State the blood parasite species.
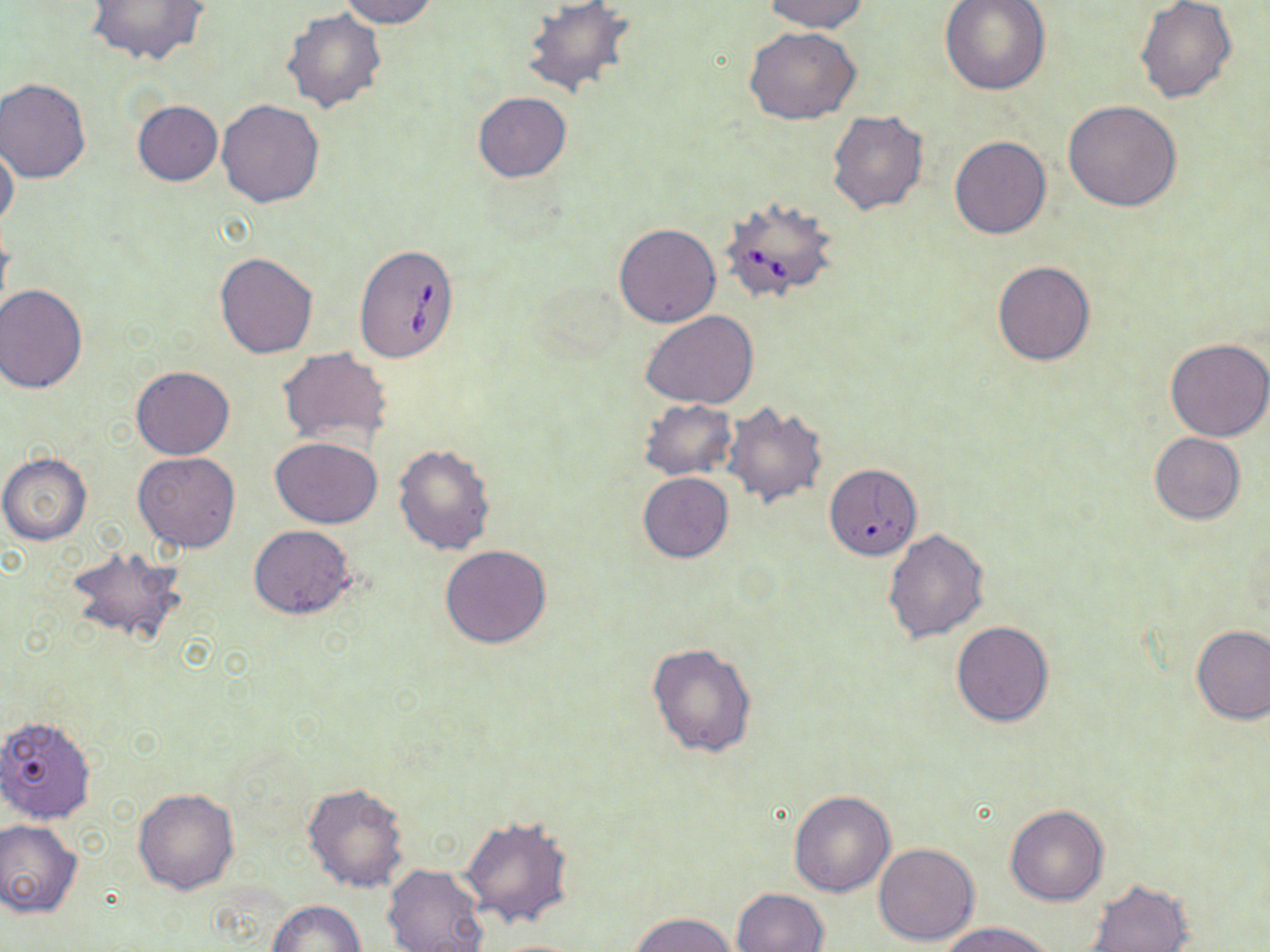

Babesia divergens.

stain = May-Grünwald-Giemsa
preparation = thin blood film
field of view = single
image size = 1270×952 pixels
Babesia divergens-infected red blood cell locations = approximate bounding boxes as (x1, y1, x2, y2) in pixels: (721, 196, 839, 305), (355, 245, 459, 363), (830, 465, 917, 557)
uninfected red blood cell locations = approximate bounding boxes as (x1, y1, x2, y2) in pixels: (85, 0, 211, 68), (337, 0, 440, 28), (760, 0, 870, 33), (939, 0, 1049, 95), (522, 1, 637, 100), (1135, 1, 1237, 104), (281, 7, 388, 112), (743, 26, 862, 123), (0, 79, 90, 183), (472, 92, 573, 183), (216, 99, 325, 207), (132, 100, 223, 186), (1063, 100, 1183, 211), (827, 110, 928, 216), (949, 136, 1051, 239), (0, 143, 20, 233), (613, 222, 722, 327), (215, 253, 317, 359), (992, 260, 1094, 366), (1, 286, 88, 393), (641, 311, 760, 410), (1165, 337, 1270, 441), (277, 346, 394, 449), (131, 365, 234, 460), (636, 399, 738, 480), (721, 401, 828, 508), (1150, 432, 1245, 524), (271, 436, 382, 528), (392, 444, 495, 555), (132, 452, 240, 552), (0, 453, 93, 544), (638, 472, 734, 563), (248, 524, 355, 618), (882, 528, 990, 645), (440, 544, 552, 648), (66, 545, 188, 648), (951, 619, 1056, 726), (1190, 624, 1269, 725), (646, 642, 758, 759), (0, 716, 100, 826), (302, 782, 409, 891), (133, 787, 239, 894), (788, 790, 896, 898), (1003, 803, 1110, 905), (459, 814, 574, 927), (0, 818, 83, 917), (873, 842, 980, 946), (382, 864, 489, 952), (1083, 878, 1193, 952), (733, 887, 829, 952), (265, 899, 365, 952), (630, 911, 740, 951), (941, 923, 1055, 952), (478, 938, 592, 951)
magnification = 1000x
modality = optical microscopy